Report the malaria status of this cell.
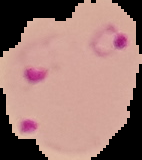

Parasitized.

Summary:
  - Image size: 142×160 pixels
  - Preparation: thin blood smear
  - Image type: cell region segmented out of the field of view; surrounding area masked to black